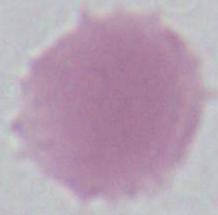 1000x magnification. A red blood cell is shown. Photomicrograph.